Locate every blood parasite and identify its species.
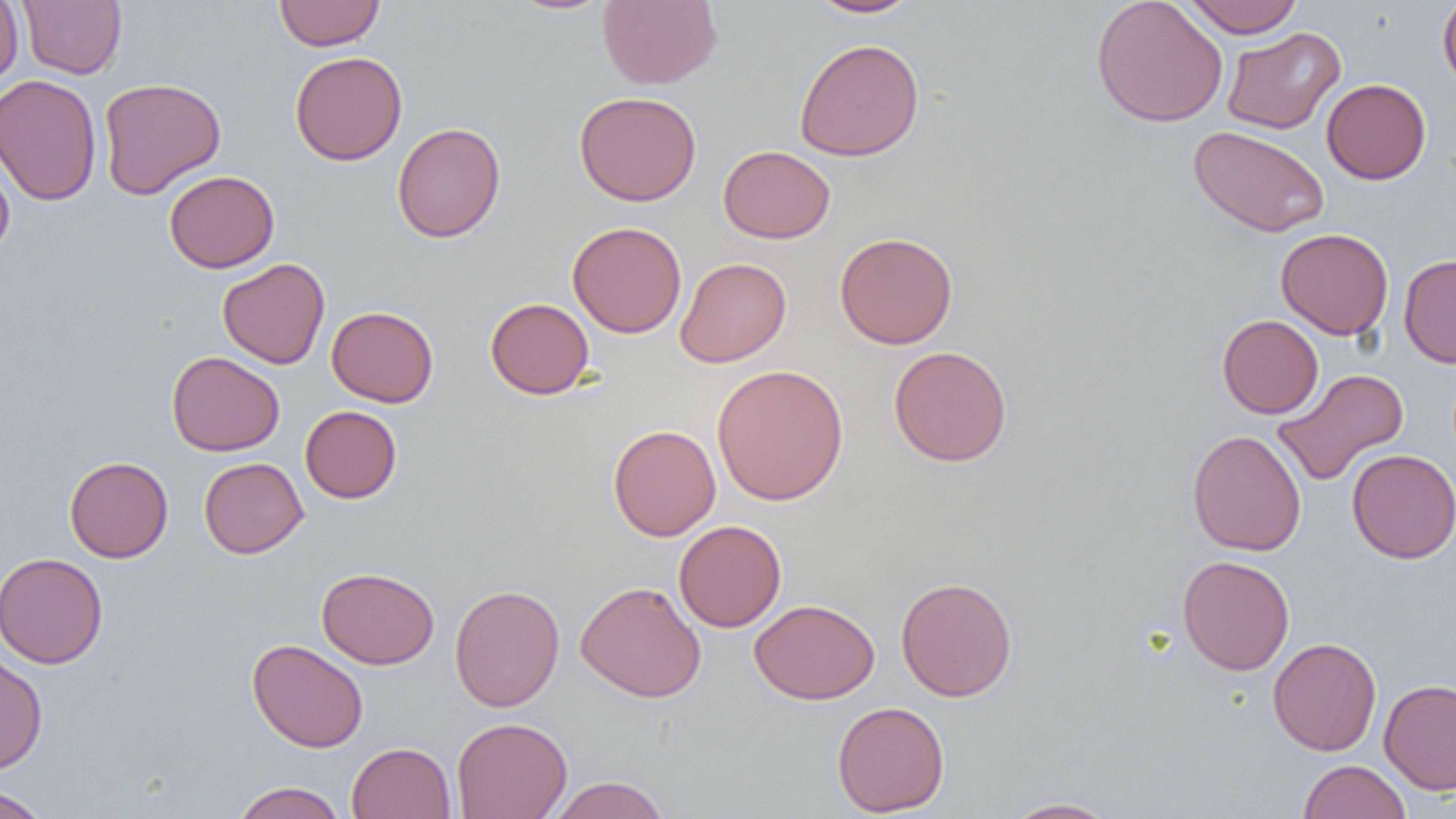
No blood parasites seen.

Approximate bounding boxes as [x1, y1, x2, y2] in pixels. Uninfected red blood cell locations: [18, 0, 127, 79], [274, 0, 385, 51], [507, 0, 615, 15], [597, 0, 722, 89], [807, 0, 920, 18], [1091, 0, 1228, 128], [1181, 0, 1305, 38], [1437, 0, 1456, 94], [0, 1, 23, 86], [1222, 27, 1345, 134], [794, 38, 925, 161], [290, 51, 408, 165], [0, 74, 102, 207], [98, 77, 226, 199], [1321, 78, 1431, 184], [574, 91, 701, 206], [392, 122, 506, 243], [1189, 125, 1330, 237], [0, 144, 15, 258], [718, 145, 836, 243], [164, 170, 280, 273], [567, 221, 687, 338], [1275, 228, 1394, 340], [834, 231, 959, 349], [1398, 254, 1456, 368], [217, 257, 330, 369], [675, 257, 791, 367], [485, 297, 595, 399], [326, 306, 439, 407], [1217, 314, 1323, 419], [888, 346, 1012, 467], [167, 350, 285, 456], [712, 364, 849, 506], [1272, 368, 1409, 487], [300, 405, 402, 503], [608, 424, 721, 541], [1187, 429, 1306, 556], [1346, 448, 1456, 564], [64, 456, 173, 563], [199, 457, 308, 558], [673, 519, 787, 632], [0, 552, 109, 669], [1177, 555, 1294, 675], [316, 567, 439, 669], [895, 576, 1017, 702], [575, 581, 706, 703], [449, 584, 565, 712], [749, 599, 880, 704], [1268, 637, 1382, 756], [247, 638, 369, 753], [0, 654, 48, 774], [1379, 678, 1456, 794], [831, 700, 949, 817], [451, 716, 573, 819], [346, 742, 456, 818], [1298, 759, 1411, 819], [546, 775, 671, 819], [231, 781, 347, 819], [0, 786, 50, 819], [999, 797, 1120, 818]. Slide-level diagnosis: negative for blood parasites. Thin blood film. Light microscopy. Single field of view. Image is 1456×819 pixels. Captured at 1000x magnification.